Report the malaria status of this cell.
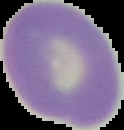
Uninfected.

{
  "image_type": "segmented cell region with the area outside set to black",
  "image_size": "124×130 pixels",
  "preparation": "thin blood smear"
}